Outline each P. falciparum parasite and classify it by life-cycle stage.
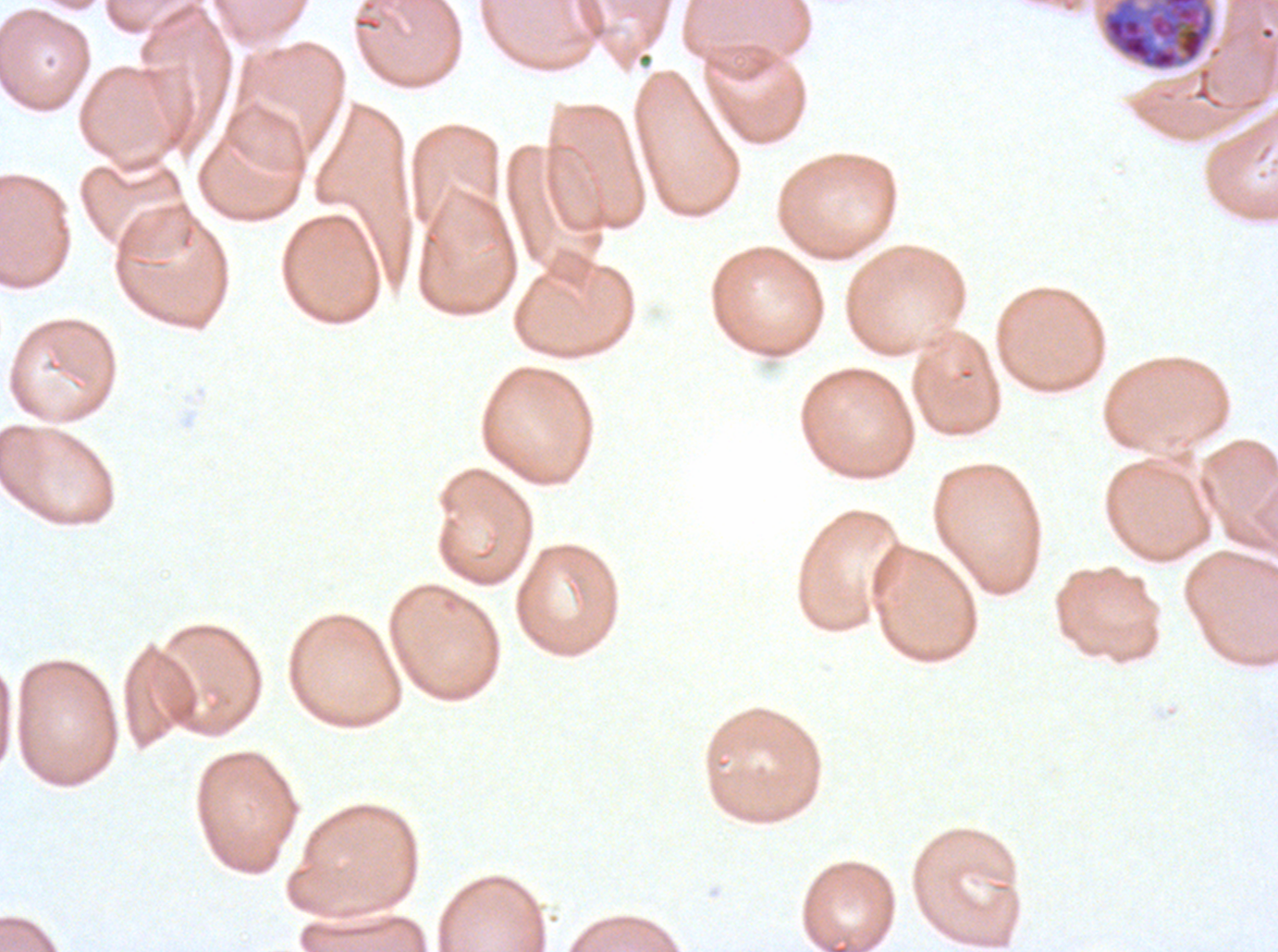
Approximate bounding boxes as {x1, y1, x2, y2} in pixels.
Late schizonts: {1101, 0, 1215, 71}.
No rings, late-ring/early-trophozoite forms, mid trophozoites, late trophozoites, early schizonts, segmenters, or gametocytes observed.

stain = Giemsa
image size = 1278×952 pixels
specimen = P. falciparum cultured ex vivo for 24 to 48 hours, from a patient in The Gambia
field of view = sub-image separated from a larger composite
preparation = thin blood film